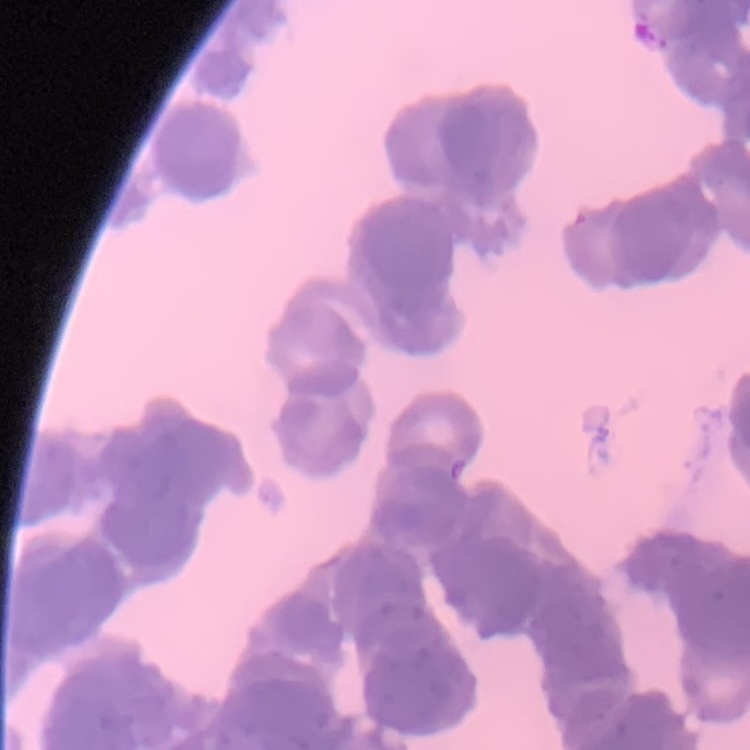

Summary:
  - Red blood cell morphology: rouleaux formation
  - Preparation: thin blood film
  - Stain: Field's or Giemsa
  - Image type: one tile cut from a larger photomicrograph